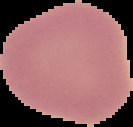

Summary:
  - Image type: cell region segmented out of the field of view; surrounding area masked to black
  - Image size: 133×127 pixels
  - Result: no Plasmodium parasites detected
  - Preparation: thin blood smear